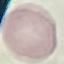

Summary:
  - Result: negative for malaria parasites
  - Image type: automatically extracted cell patch, resized to 64 × 64 pixels
  - Capture: smartphone through the microscope eyepiece
  - Preparation: thin blood film
  - Stain: Giemsa